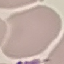

malaria status = uninfected
stain = Giemsa
image type = automatically extracted cell patch, resized to 64 × 64 pixels
preparation = thin blood film
capture = smartphone camera at the microscope eyepiece